Report the malaria status of this cell.
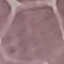
Uninfected.

stain = Giemsa
preparation = thin blood film
capture = smartphone through the microscope eyepiece
image type = automatically extracted cell patch, resized to 64 × 64 pixels